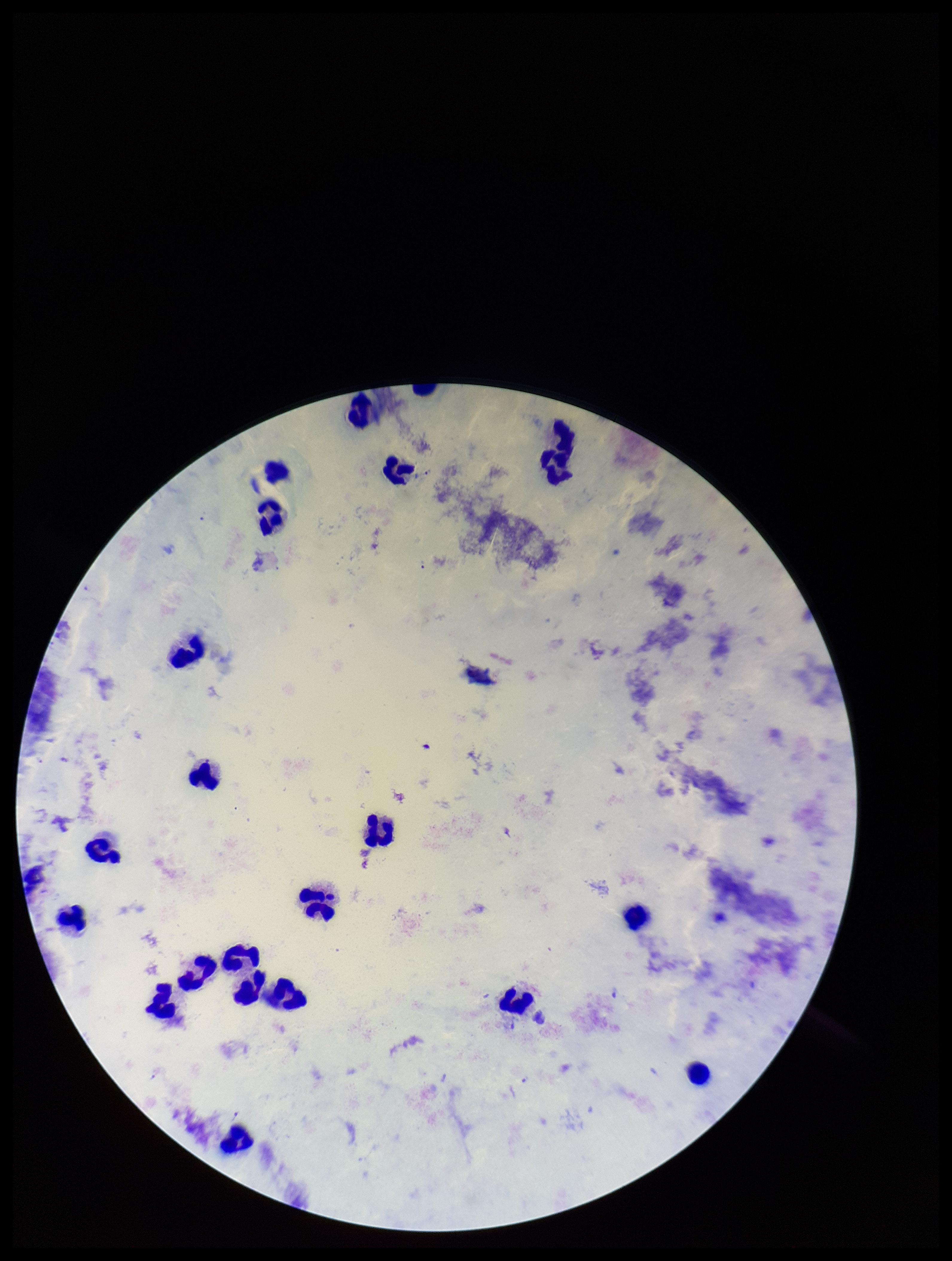

Preparation: thick. Parasite count: 1. Giemsa stain. Leukocyte count: 22. Patient malaria status: positive. Photographed through the microscope eyepiece with a smartphone camera. Species reported for this patient: Plasmodium falciparum. Single field of view. Plasmodium parasites: seen. Image is 952×1261 pixels.